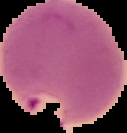
preparation = thin blood film
malaria status = parasitized
image type = cell region segmented out of the field of view; surrounding area masked to black
image size = 127×133 pixels